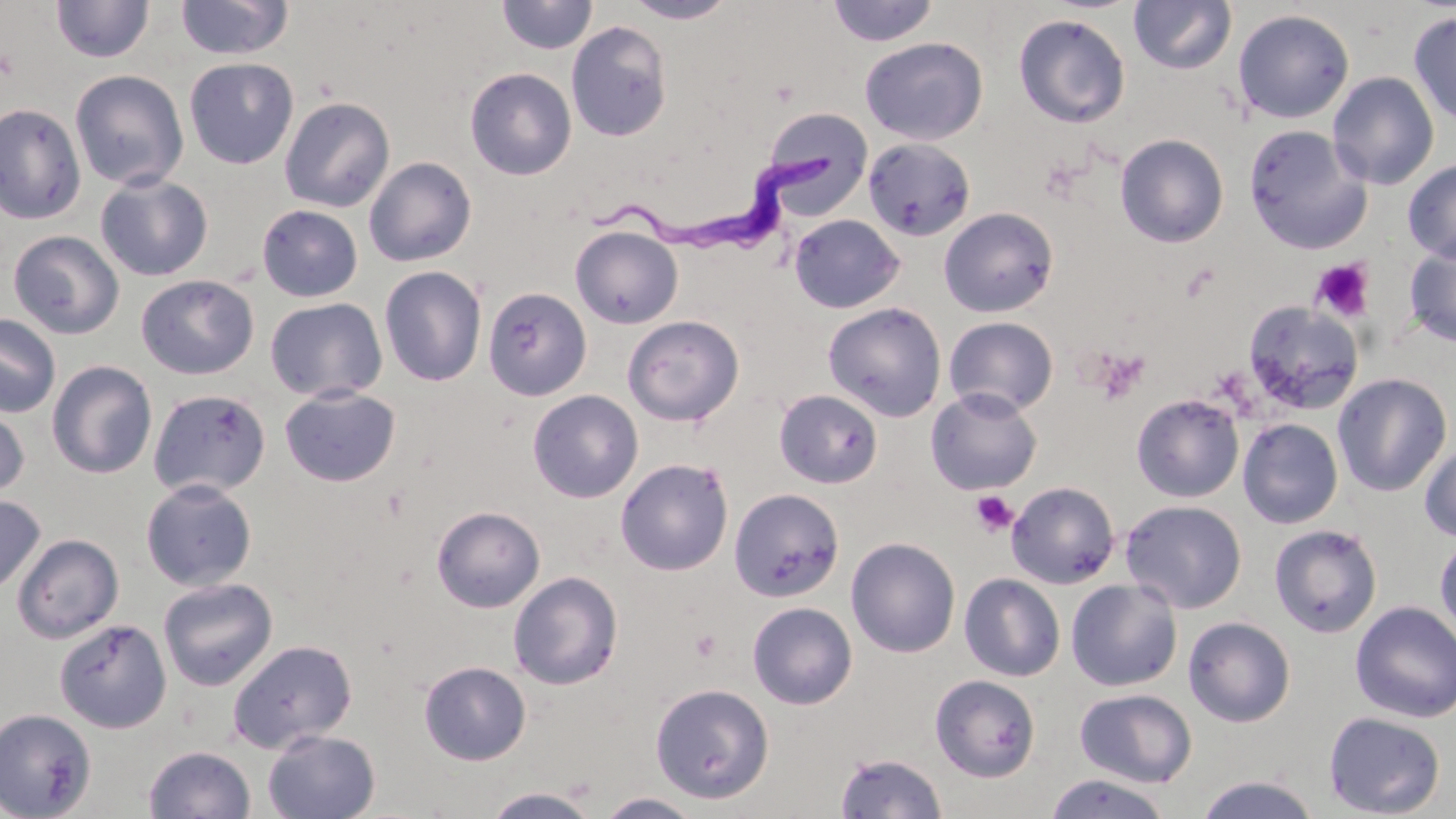
slide-level diagnosis = Trypanosoma brucei
preparation = thin blood film
image size = 1456×819 pixels
field of view = single
magnification = 1000x
Trypanosoma brucei locations = approximate bounding boxes as named x1/y1/x2/y2 corners in pixels: (x1=589, y1=151, x2=838, y2=266)
modality = optical microscopy
uninfected red blood cell locations = approximate bounding boxes as named x1/y1/x2/y2 corners in pixels: (x1=175, y1=0, x2=293, y2=60), (x1=495, y1=0, x2=598, y2=55), (x1=826, y1=0, x2=939, y2=47), (x1=50, y1=1, x2=154, y2=63), (x1=623, y1=1, x2=737, y2=23), (x1=1129, y1=1, x2=1236, y2=74), (x1=1233, y1=9, x2=1355, y2=124), (x1=1408, y1=10, x2=1456, y2=126), (x1=1013, y1=14, x2=1130, y2=128), (x1=566, y1=20, x2=672, y2=142), (x1=860, y1=36, x2=988, y2=145), (x1=184, y1=57, x2=299, y2=169), (x1=464, y1=67, x2=577, y2=180), (x1=70, y1=69, x2=189, y2=191), (x1=1327, y1=71, x2=1439, y2=190), (x1=279, y1=96, x2=395, y2=213), (x1=0, y1=103, x2=86, y2=224), (x1=758, y1=107, x2=875, y2=219), (x1=1242, y1=124, x2=1371, y2=253), (x1=1115, y1=134, x2=1229, y2=248), (x1=863, y1=137, x2=976, y2=241), (x1=364, y1=156, x2=477, y2=267), (x1=1403, y1=159, x2=1456, y2=263), (x1=95, y1=173, x2=213, y2=281), (x1=256, y1=204, x2=363, y2=302), (x1=938, y1=207, x2=1058, y2=317), (x1=788, y1=214, x2=905, y2=313), (x1=570, y1=225, x2=683, y2=328), (x1=8, y1=230, x2=124, y2=340), (x1=1403, y1=238, x2=1456, y2=347), (x1=379, y1=266, x2=487, y2=387), (x1=136, y1=274, x2=258, y2=380), (x1=482, y1=287, x2=592, y2=401), (x1=265, y1=298, x2=387, y2=402), (x1=1242, y1=301, x2=1364, y2=415), (x1=823, y1=302, x2=947, y2=421), (x1=0, y1=314, x2=61, y2=418), (x1=623, y1=315, x2=744, y2=426), (x1=943, y1=316, x2=1059, y2=417), (x1=47, y1=360, x2=157, y2=479), (x1=1332, y1=373, x2=1453, y2=497), (x1=279, y1=386, x2=401, y2=487), (x1=925, y1=387, x2=1042, y2=495), (x1=148, y1=388, x2=271, y2=499), (x1=527, y1=389, x2=643, y2=503), (x1=774, y1=389, x2=883, y2=488), (x1=1131, y1=394, x2=1244, y2=503), (x1=0, y1=401, x2=30, y2=501), (x1=1237, y1=418, x2=1343, y2=529), (x1=1419, y1=437, x2=1456, y2=542), (x1=614, y1=458, x2=734, y2=576), (x1=140, y1=479, x2=257, y2=591), (x1=1006, y1=481, x2=1120, y2=589), (x1=729, y1=489, x2=844, y2=602), (x1=0, y1=494, x2=45, y2=596), (x1=1120, y1=500, x2=1247, y2=614), (x1=431, y1=505, x2=546, y2=613), (x1=1269, y1=523, x2=1383, y2=638), (x1=1434, y1=533, x2=1456, y2=644), (x1=11, y1=534, x2=124, y2=643), (x1=846, y1=537, x2=961, y2=658), (x1=508, y1=570, x2=624, y2=690), (x1=959, y1=574, x2=1066, y2=682), (x1=158, y1=577, x2=278, y2=692), (x1=1066, y1=579, x2=1183, y2=691), (x1=747, y1=601, x2=857, y2=709), (x1=1350, y1=601, x2=1456, y2=723), (x1=1183, y1=616, x2=1296, y2=727), (x1=54, y1=617, x2=172, y2=733), (x1=227, y1=638, x2=357, y2=753), (x1=419, y1=661, x2=531, y2=765), (x1=930, y1=674, x2=1041, y2=782), (x1=650, y1=683, x2=774, y2=803), (x1=1074, y1=688, x2=1197, y2=788), (x1=0, y1=709, x2=96, y2=819), (x1=1323, y1=711, x2=1446, y2=818), (x1=262, y1=729, x2=380, y2=819), (x1=144, y1=746, x2=256, y2=819), (x1=835, y1=753, x2=948, y2=819), (x1=1042, y1=772, x2=1174, y2=818), (x1=1194, y1=774, x2=1321, y2=818), (x1=483, y1=788, x2=599, y2=818), (x1=595, y1=792, x2=705, y2=819)
platelet locations = approximate bounding boxes as named x1/y1/x2/y2 corners in pixels: (x1=1311, y1=258, x2=1376, y2=323), (x1=1092, y1=347, x2=1149, y2=404), (x1=969, y1=491, x2=1018, y2=537), (x1=690, y1=627, x2=722, y2=663)
stain = May-Grünwald-Giemsa